Locate every Plasmodium parasite.
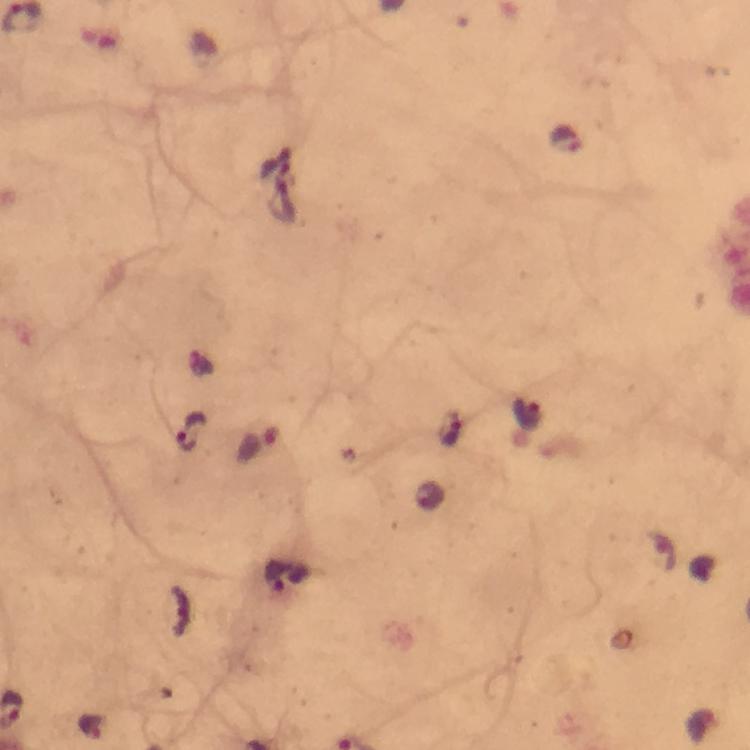
Approximate centers as (x, y) in pixels.
Plasmodium parasites: (565, 142), (526, 414), (448, 428), (192, 432), (258, 443), (90, 727).

Summary:
  - Capture: smartphone mounted on the microscope
  - Cropped from: one field of view
  - Immersion oil: applied
  - Magnification: 100x
  - Context: from a malaria diagnostic workup
  - Stain: Giemsa
  - Image size: 750×750 pixels
  - Preparation: thick blood smear